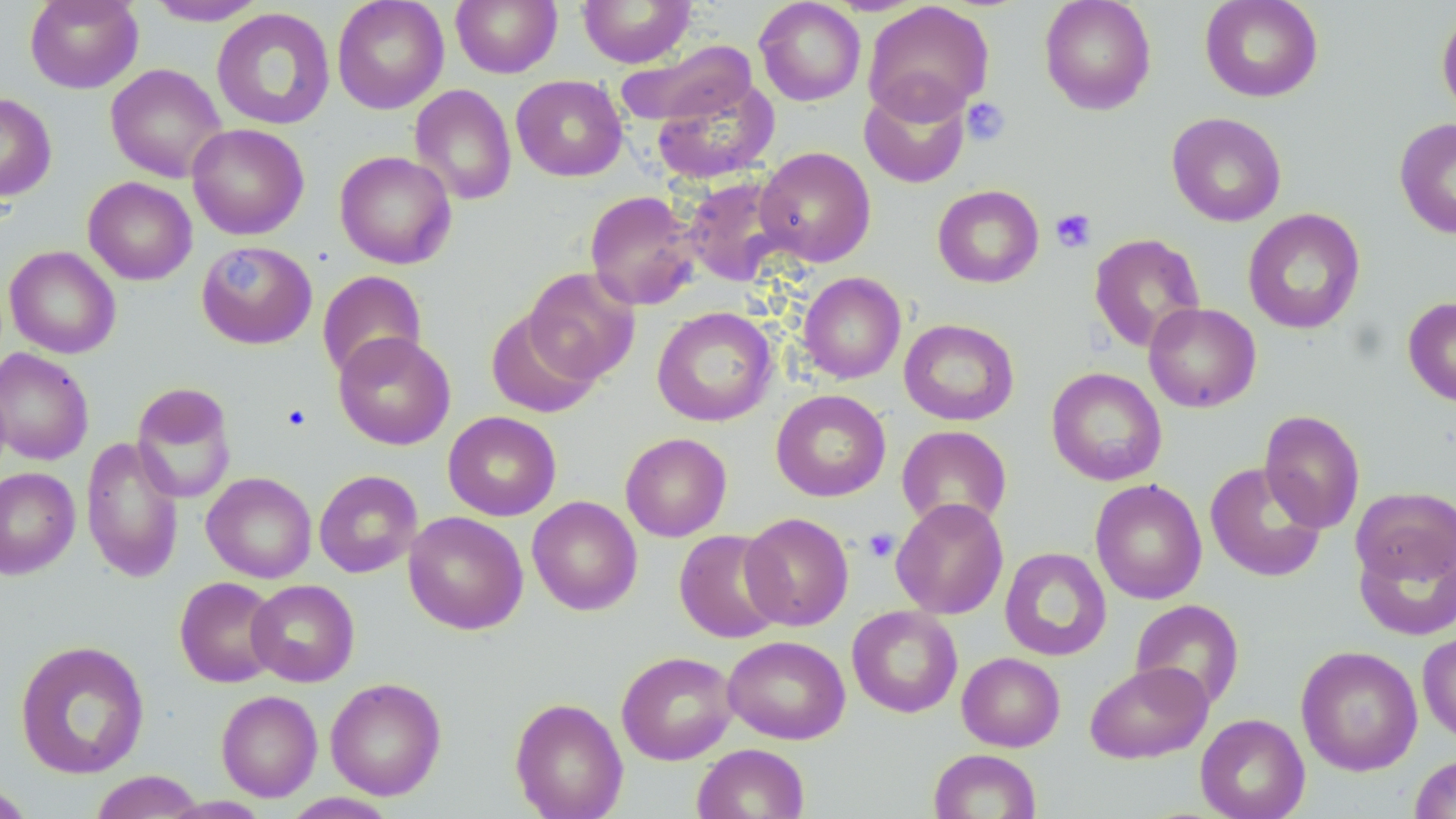
Summary:
  - Coordinate format: approximate bounding boxes as (x1, y1, x2, y2) in pixels
  - Platelet locations: (962, 97, 1011, 145), (1050, 208, 1096, 253), (281, 403, 311, 432), (863, 527, 899, 562)
  - Uninfected red blood cell locations: (25, 0, 143, 93), (146, 0, 268, 25), (332, 0, 449, 114), (577, 0, 696, 68), (1039, 0, 1157, 115), (1199, 0, 1324, 102), (451, 1, 561, 78), (754, 1, 867, 106), (863, 2, 994, 122), (211, 7, 336, 130), (1436, 9, 1456, 122), (615, 39, 758, 130), (105, 63, 227, 183), (511, 75, 628, 181), (651, 80, 778, 185), (859, 82, 971, 189), (409, 85, 517, 205), (0, 93, 56, 201), (1167, 112, 1287, 227), (1394, 118, 1456, 241), (187, 123, 309, 240), (755, 146, 876, 267), (334, 151, 456, 270), (682, 174, 799, 286), (83, 177, 197, 285), (932, 184, 1044, 288), (585, 190, 701, 310), (1243, 208, 1366, 334), (1089, 233, 1205, 353), (196, 241, 317, 350), (4, 245, 120, 358), (522, 267, 640, 385), (316, 270, 427, 381), (798, 272, 906, 383), (1403, 297, 1456, 407), (1144, 302, 1261, 413), (652, 307, 777, 426), (486, 309, 602, 418), (899, 318, 1019, 426), (333, 331, 456, 450), (0, 347, 94, 465), (1046, 367, 1167, 487), (131, 383, 237, 504), (771, 389, 891, 502), (1260, 409, 1365, 533), (443, 411, 561, 521), (897, 425, 1012, 531), (620, 433, 732, 542), (80, 436, 184, 583), (1204, 461, 1327, 582), (0, 467, 80, 579), (314, 470, 423, 578), (202, 471, 317, 583), (1090, 478, 1207, 605), (1351, 487, 1456, 585), (527, 495, 642, 616), (891, 498, 1008, 619), (403, 511, 528, 634), (740, 513, 854, 631), (674, 529, 787, 644), (1354, 534, 1456, 641), (999, 547, 1112, 661), (174, 577, 282, 688), (246, 579, 359, 687), (1130, 599, 1245, 711), (846, 605, 963, 718), (1417, 631, 1456, 744), (723, 635, 850, 744), (14, 639, 150, 780), (1296, 645, 1423, 776), (616, 651, 738, 764), (957, 652, 1065, 751), (1085, 661, 1213, 763), (325, 678, 446, 800), (216, 690, 322, 802), (510, 697, 628, 819), (1195, 713, 1310, 819), (692, 743, 810, 819), (928, 749, 1041, 819), (1408, 754, 1456, 818), (90, 770, 205, 819), (0, 781, 37, 818), (281, 792, 401, 818), (160, 796, 273, 819)
  - Slide-level diagnosis: negative for blood parasites
  - Field of view: single
  - Preparation: thin blood film
  - Magnification: 1000x
  - Modality: optical microscopy
  - Stain: May-Grünwald-Giemsa
  - Image size: 1456×819 pixels